Assess the background quality.
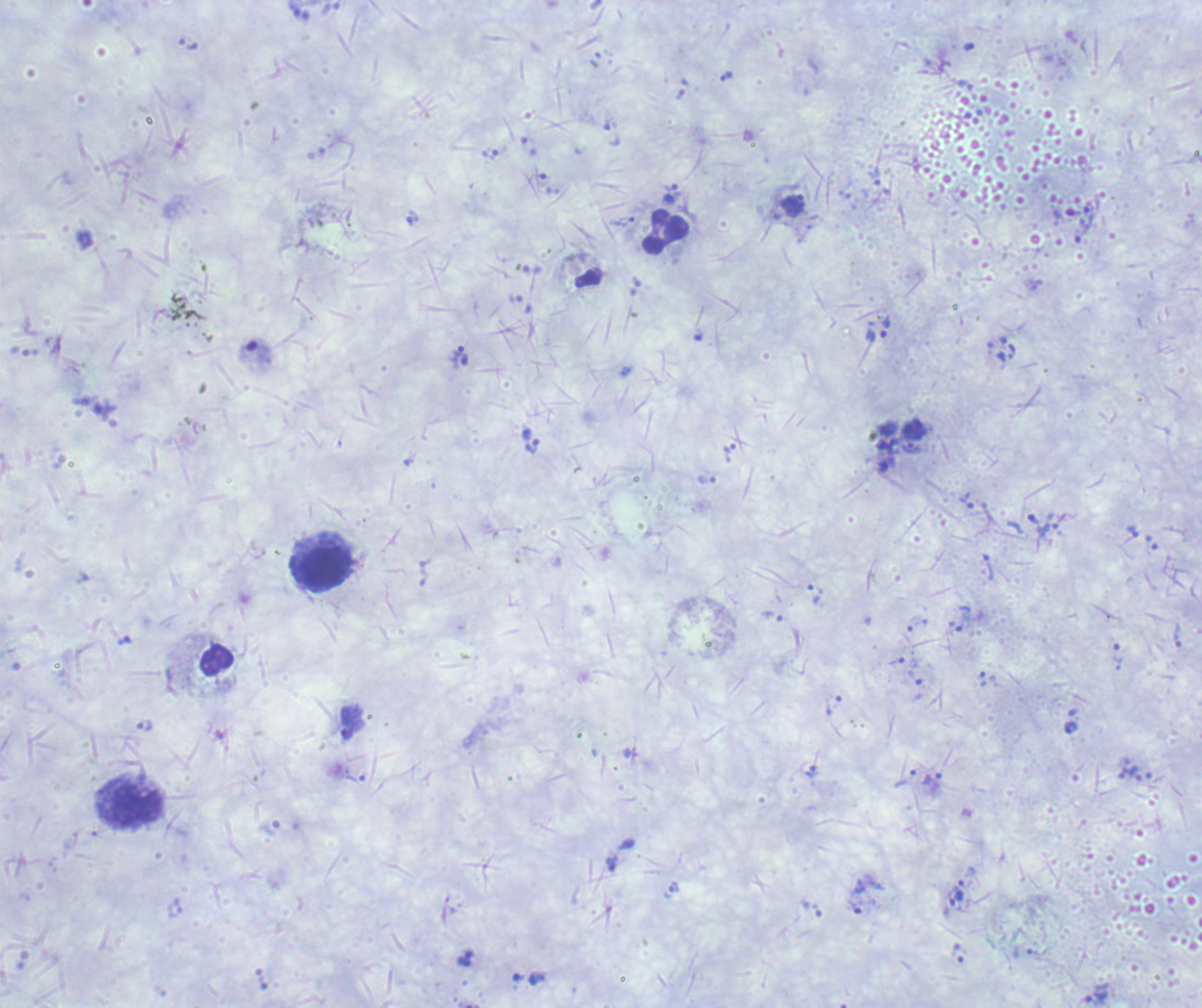
It is poor.

coordinate format = approximate centers as {x, y} in pixels
trophozoite locations = {188, 45}, {969, 47}, {727, 76}, {792, 205}, {623, 222}, {533, 447}, {911, 448}, {731, 449}, {967, 500}, {1033, 519}, {987, 566}, {813, 594}, {1178, 635}, {982, 679}, {346, 722}, {1070, 727}, {933, 777}, {612, 864}, {674, 888}, {959, 891}, {958, 953}, {465, 960}, {518, 978}
leukocyte locations = {666, 232}, {324, 569}, {138, 805}
image size = 1202×1008 pixels
field of view = one from this slide
preparation = thick blood film
stain = Romanowsky
context = previously used in an actual diagnosis
result = Plasmodium parasites identified
magnification = 100x